Look for Plasmodium parasites.
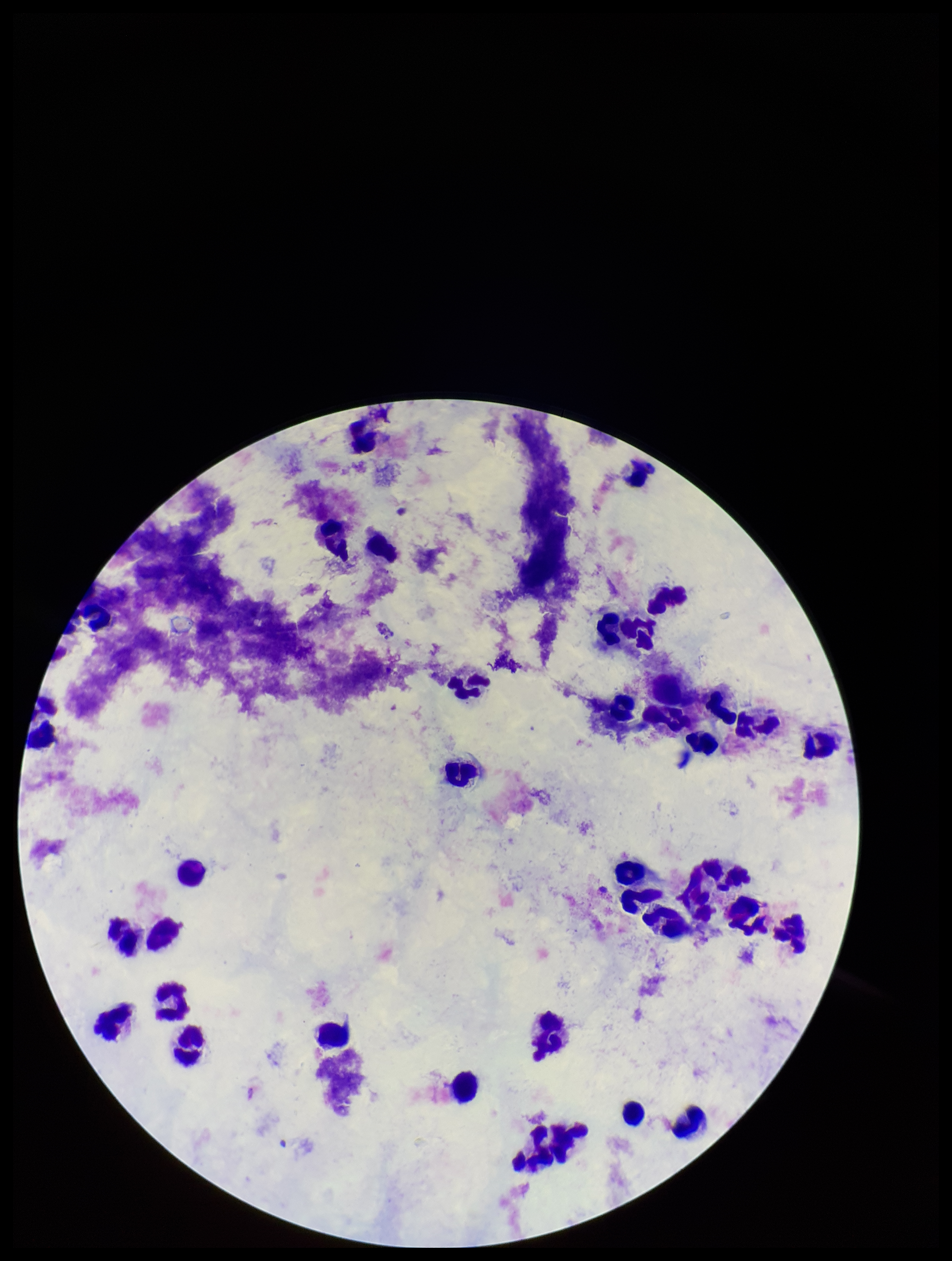
None seen.

{
  "patient_malaria_status": "negative",
  "field_of_view": "one from this slide",
  "capture": "smartphone photograph through the microscope eyepiece",
  "parasite_count": 0,
  "stain": "Giemsa",
  "leukocyte_count": 37,
  "image_size": "952×1261 pixels",
  "preparation": "thick"
}